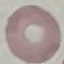 Malaria status: uninfected. Giemsa stain. Thin blood film. Cell patch, automatically extracted from a larger field of view and resized to 64 × 64 pixels. Photographed with a smartphone camera at the microscope eyepiece.